Name the blood parasite species.
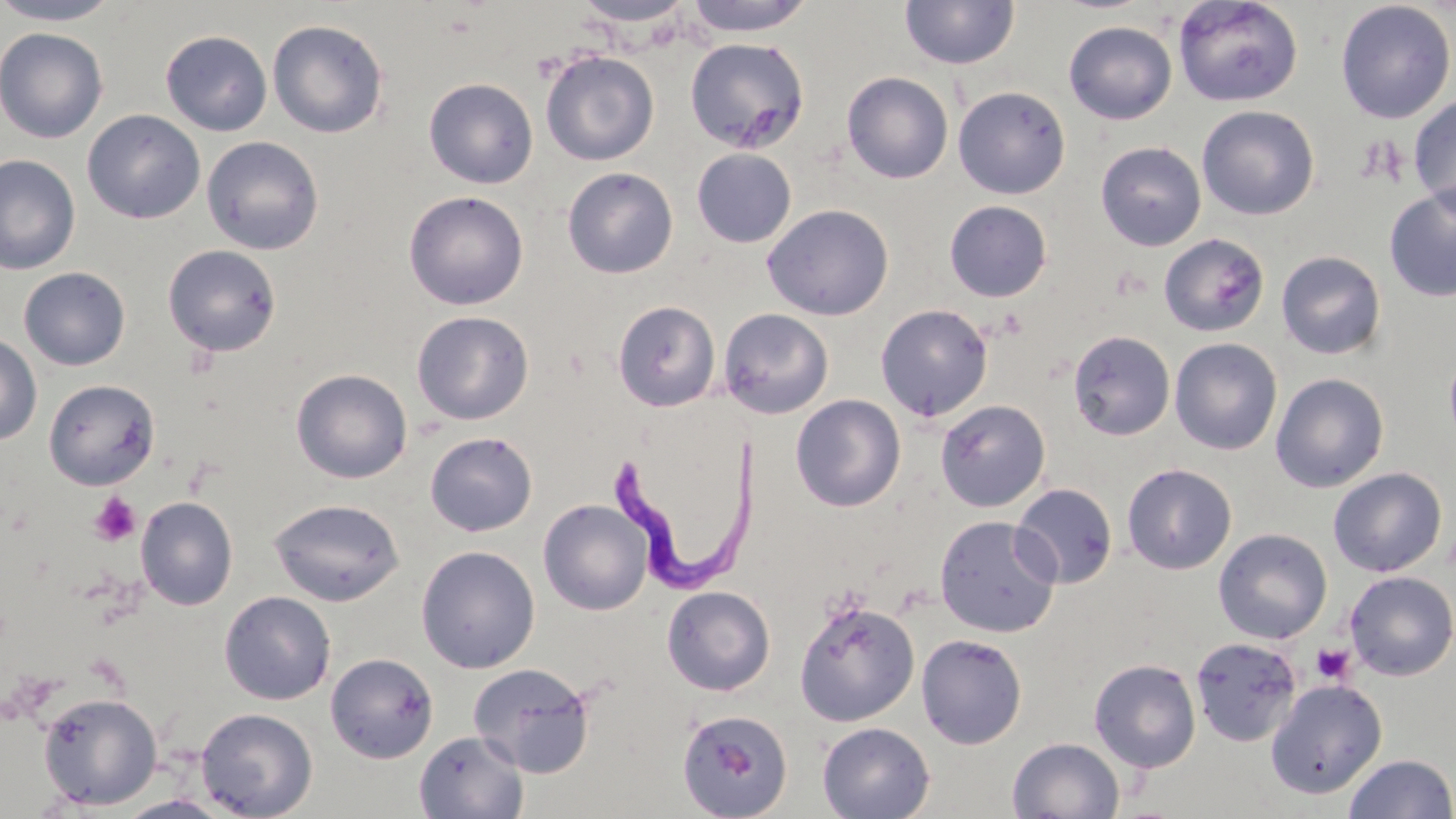
Trypanosoma brucei.

preparation = thin blood film
platelet locations = approximate bounding boxes as (x1, y1, x2, y2) in pixels: (89, 491, 142, 547), (1310, 642, 1356, 684)
field of view = single
uninfected red blood cell locations = approximate bounding boxes as (x1, y1, x2, y2) in pixels: (0, 0, 122, 26), (682, 0, 816, 37), (900, 0, 1019, 70), (1173, 0, 1303, 107), (571, 1, 695, 29), (1335, 1, 1455, 123), (268, 19, 389, 139), (1064, 20, 1177, 124), (0, 26, 108, 144), (160, 29, 273, 136), (684, 38, 810, 154), (540, 49, 659, 166), (841, 71, 954, 184), (423, 78, 538, 189), (952, 85, 1071, 199), (1408, 95, 1456, 215), (1196, 105, 1320, 221), (82, 109, 205, 224), (201, 135, 324, 255), (1095, 141, 1207, 251), (691, 148, 797, 248), (0, 154, 80, 275), (562, 166, 678, 279), (1384, 185, 1456, 302), (404, 190, 529, 310), (944, 200, 1052, 302), (762, 203, 894, 321), (1158, 233, 1269, 336), (163, 244, 282, 356), (1276, 250, 1386, 360), (19, 267, 131, 370), (612, 301, 720, 412), (875, 303, 994, 421), (718, 308, 834, 419), (411, 310, 534, 426), (1067, 330, 1175, 441), (0, 333, 42, 446), (1169, 338, 1283, 455), (1444, 344, 1456, 450), (291, 369, 412, 483), (1270, 372, 1390, 493), (44, 379, 160, 490), (791, 394, 905, 511), (935, 399, 1050, 511), (425, 431, 538, 537), (1121, 463, 1237, 574), (1328, 467, 1447, 577), (1011, 483, 1118, 588), (135, 496, 238, 610), (268, 497, 406, 606), (538, 499, 653, 615), (935, 514, 1060, 637), (1213, 528, 1332, 644), (416, 545, 540, 673), (1344, 570, 1456, 681), (661, 585, 776, 696), (219, 590, 336, 705), (793, 598, 920, 727), (916, 633, 1027, 749), (1190, 636, 1302, 746), (325, 652, 439, 763), (1089, 658, 1201, 773), (468, 663, 597, 779), (1265, 679, 1387, 799), (37, 691, 162, 810), (195, 707, 318, 819), (676, 709, 794, 819), (817, 722, 935, 819), (414, 730, 528, 818), (1007, 737, 1125, 818), (1343, 753, 1456, 819), (115, 795, 235, 819)
Trypanosoma brucei locations = approximate bounding boxes as (x1, y1, x2, y2) in pixels: (612, 412, 757, 590)
magnification = 1000x
modality = light microscopy
image size = 1456×819 pixels
stain = May-Grünwald-Giemsa